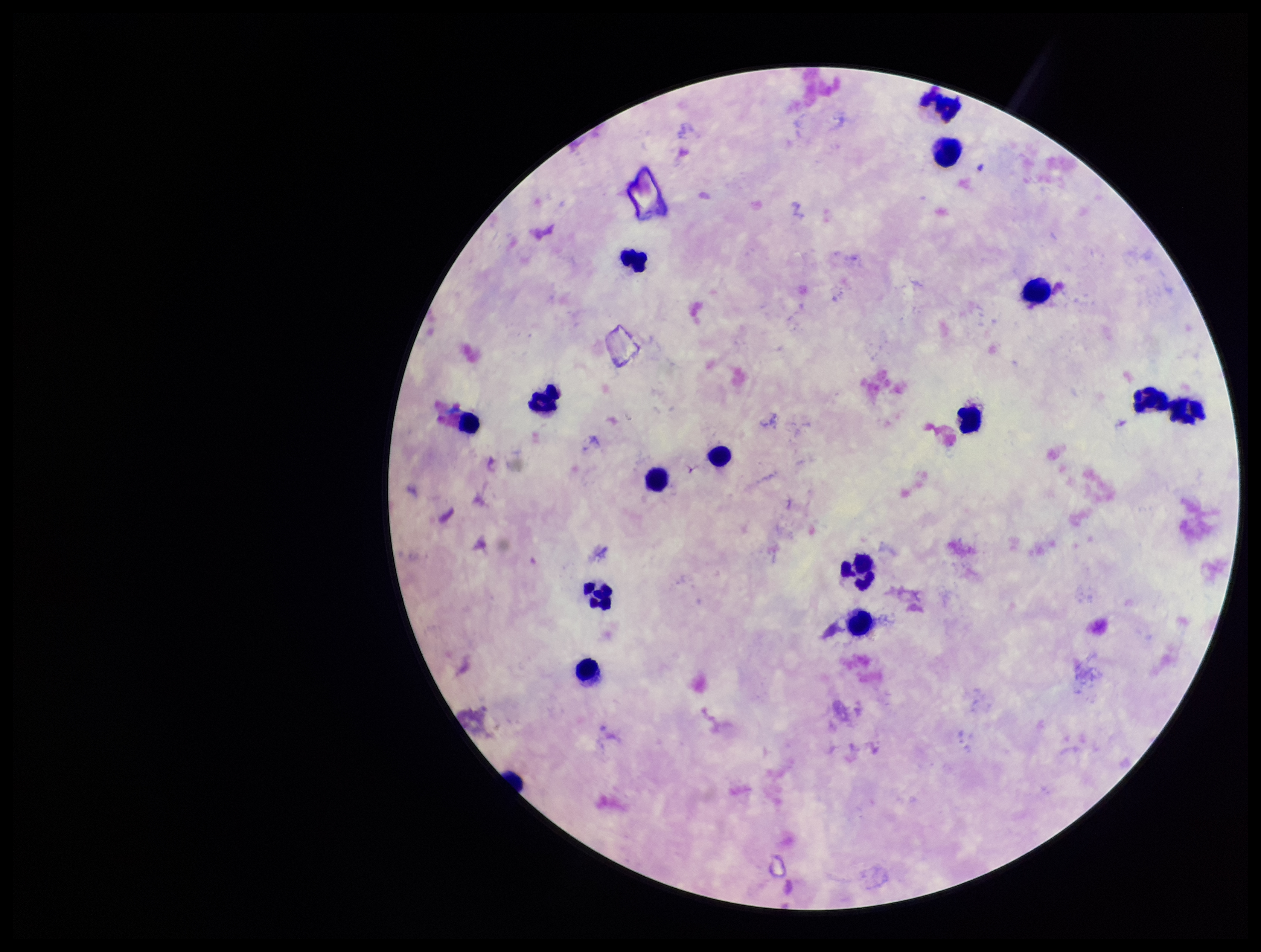
Summary:
  - Preparation: thick smear
  - Parasite count: 0
  - Field of view: one from this slide
  - Leukocyte count: 15
  - Capture: smartphone photograph through the microscope eyepiece
  - Plasmodium parasites: none detected
  - Stain: Giemsa
  - Image size: 1261×952 pixels
  - Patient malaria status: negative